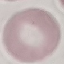
result: negative for malaria parasites
image_type: automatically extracted cell patch, resized to 64 × 64 pixels
preparation: thin smear
capture: smartphone camera at the microscope eyepiece
stain: Giemsa